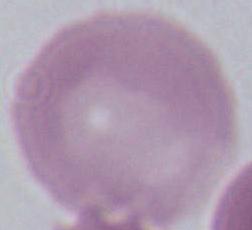 Captured at 1000x magnification. Photomicrograph. An erythrocyte is seen.